Comment on the morphology of the erythrocytes.
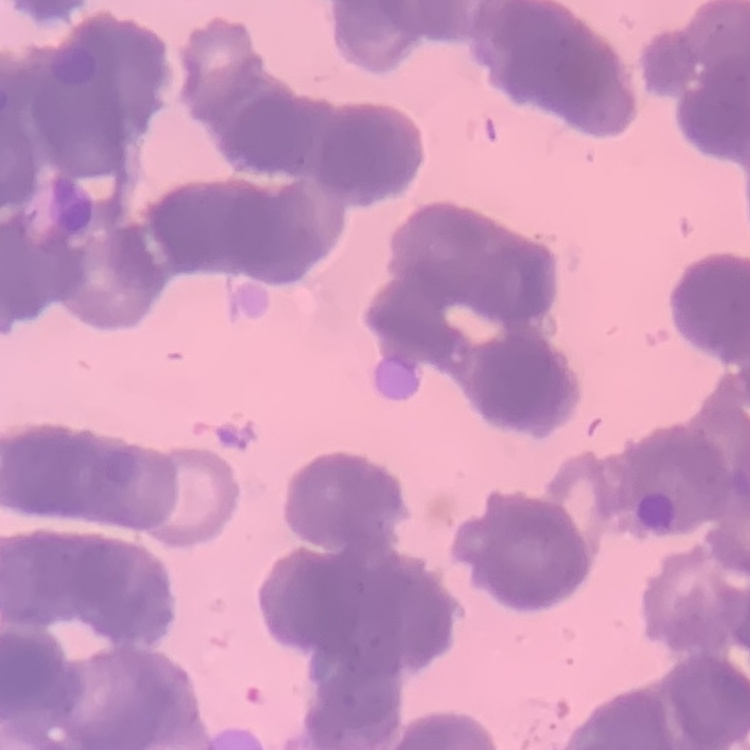

Rouleaux formation.

Summary:
  - Image type: square crop of a larger photomicrograph
  - Preparation: thin peripheral smear
  - Stain: Field's or Giemsa